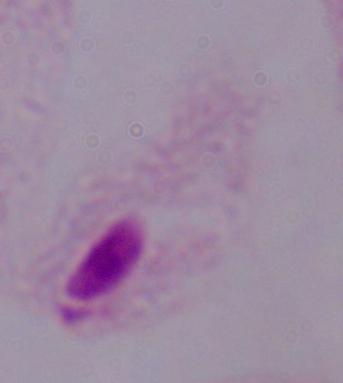
1000x magnification. A trichomonad is seen. Photomicrograph.